Name the parasite shown.
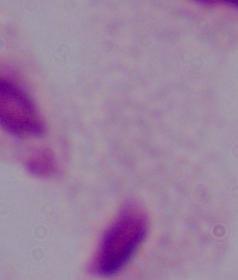

This is a trichomonad.

modality = micrograph
magnification = 1000x